Give the extent of all uninfected red blood cells.
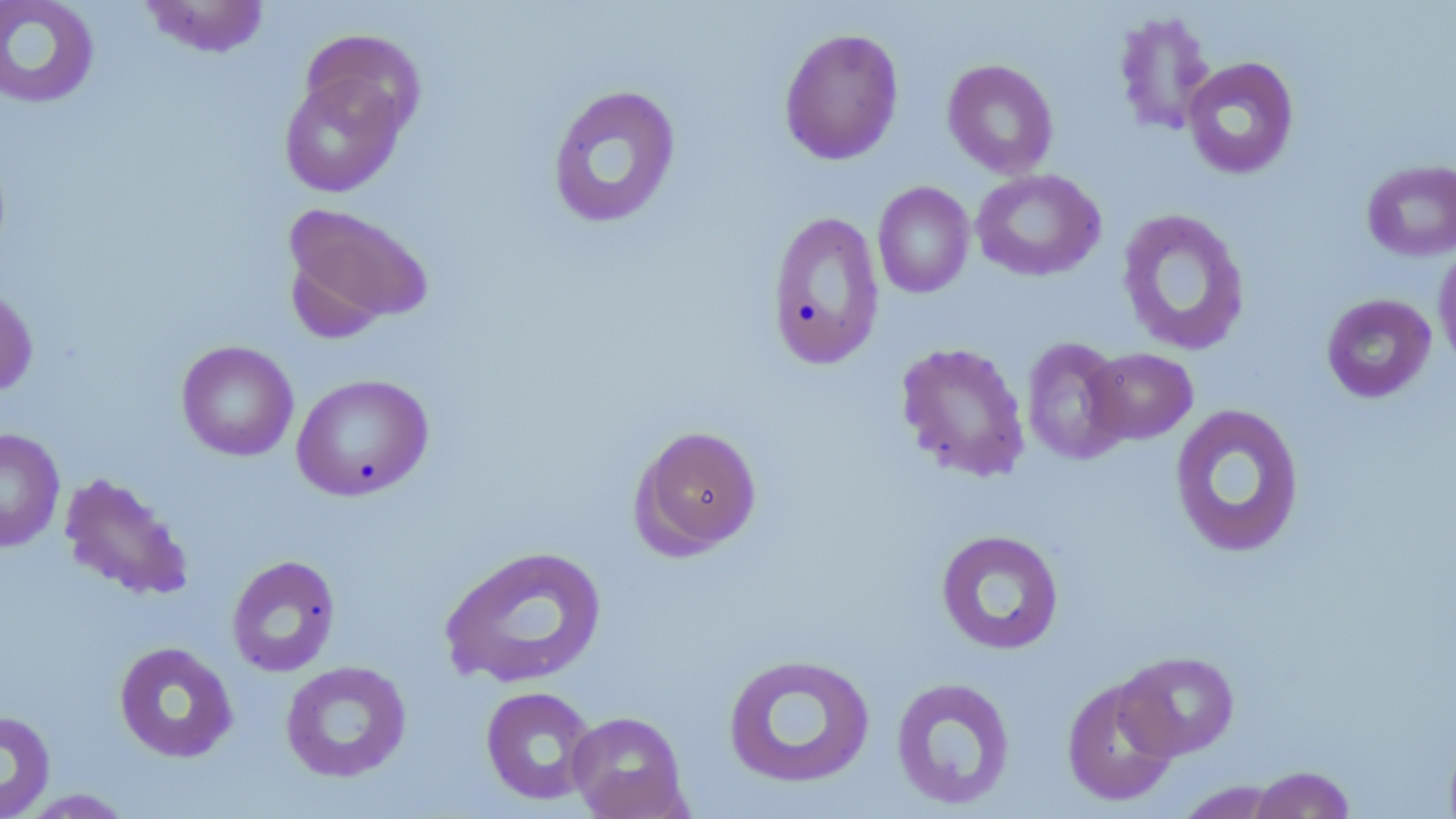
Approximate bounding boxes as (x1, y1, x2, y2) in pixels.
Uninfected red blood cells: (0, 0, 100, 109), (138, 0, 272, 58), (1113, 10, 1217, 136), (778, 27, 904, 165), (301, 29, 425, 139), (1182, 56, 1299, 180), (942, 58, 1059, 179), (278, 72, 407, 198), (546, 84, 682, 230), (1361, 159, 1456, 262), (970, 168, 1106, 281), (873, 181, 974, 298), (281, 202, 434, 337), (1116, 208, 1251, 357), (766, 210, 885, 369), (1433, 243, 1456, 372), (0, 284, 38, 398), (1321, 293, 1437, 403), (1021, 336, 1131, 466), (176, 340, 299, 462), (895, 341, 1031, 483), (1083, 347, 1198, 445), (291, 374, 434, 501), (1169, 403, 1306, 559), (630, 424, 763, 557), (0, 428, 65, 553), (58, 472, 195, 603), (935, 529, 1065, 655), (439, 544, 608, 689), (226, 554, 341, 677), (113, 641, 239, 763), (1115, 650, 1241, 760), (722, 652, 876, 789), (280, 660, 412, 783), (889, 676, 1017, 811), (1061, 677, 1180, 807), (480, 685, 599, 806), (0, 710, 55, 819), (567, 711, 689, 819), (1247, 765, 1357, 819), (1173, 780, 1289, 818), (16, 789, 136, 818).

Slide-level diagnosis: no evidence of blood parasites. Captured at 1000x magnification. Thin blood film. May-Grünwald-Giemsa-stained preparation. Image is 1456×819 pixels. Single field of view. Light microscopy.